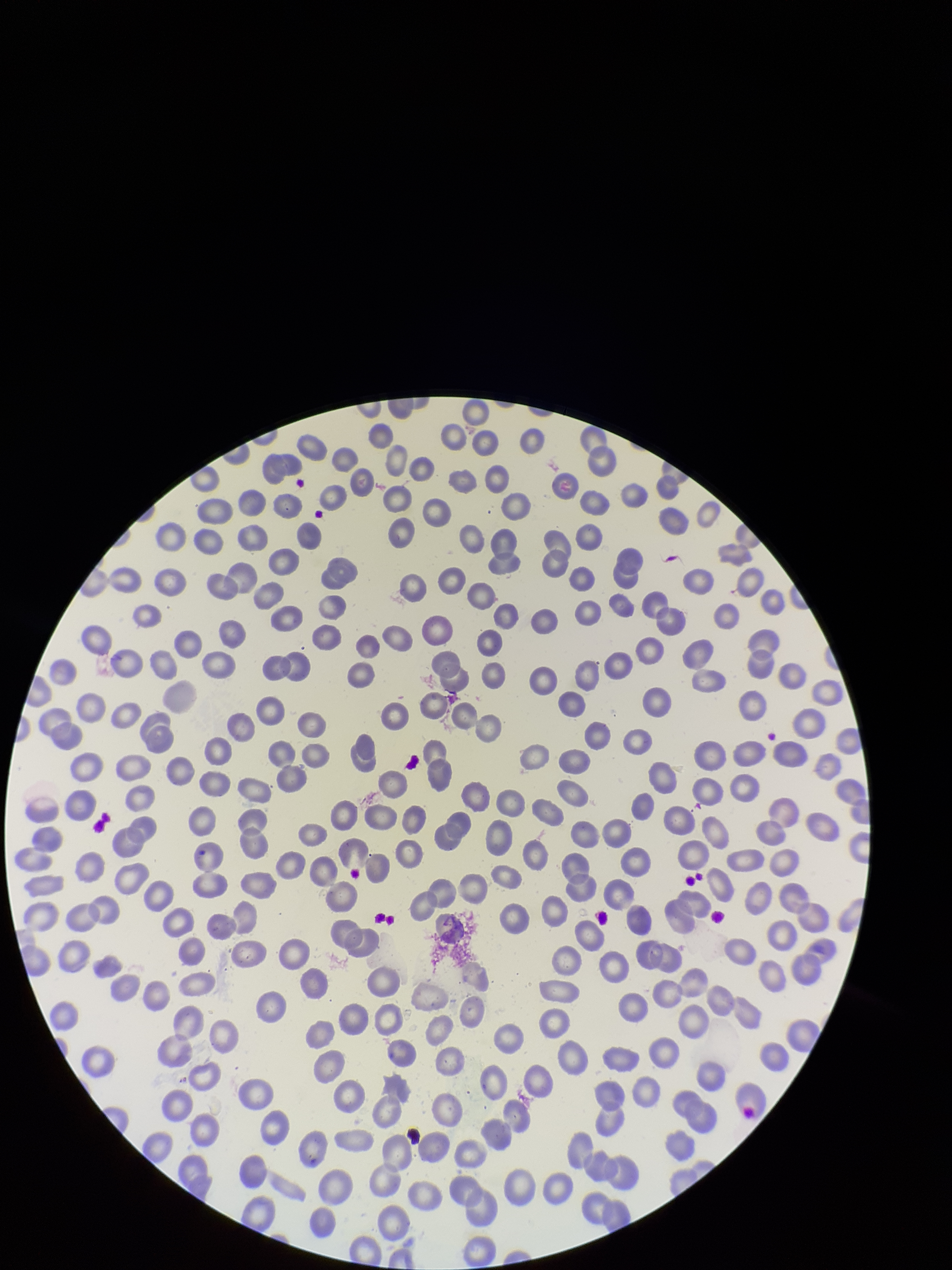
Summary:
  - Parasitized red blood cell count: 0
  - Capture: smartphone photograph through the microscope eyepiece
  - Stain: Giemsa
  - Red blood cell count: 278
  - Patient malaria status: negative
  - Field of view: single
  - Parasitized red blood cells: none detected
  - Image size: 952×1270 pixels
  - Preparation: thin smear